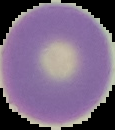 Image is 115×130 pixels. Segmented cell region on a black background. Result: no Plasmodium parasites detected. From a thin blood film.